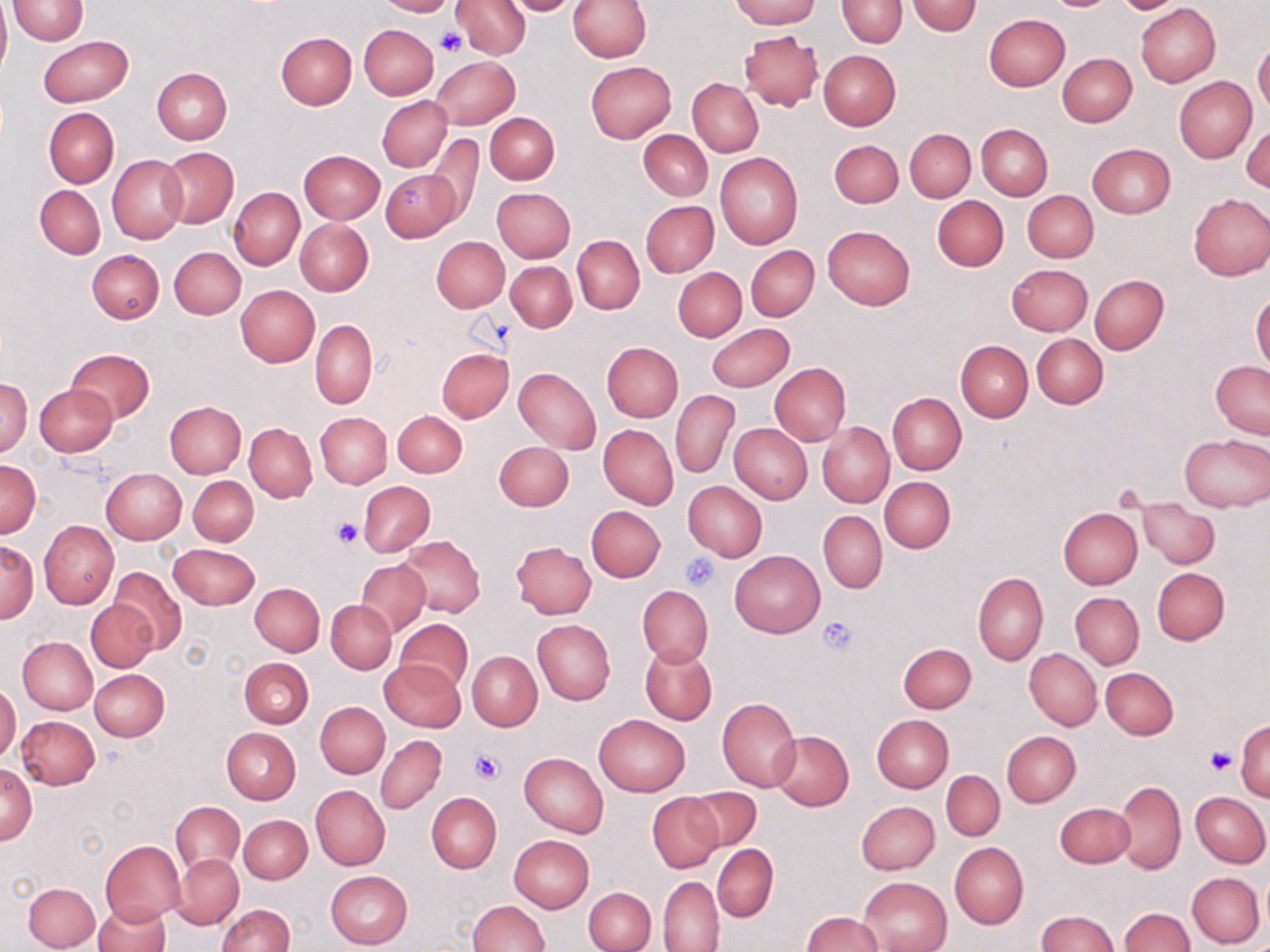
slide_level_diagnosis: negative for blood parasites
preparation: thin blood smear
stain: May-Grünwald-Giemsa
magnification: 1000x
image_size: 1270×952 pixels
field_of_view: one of a larger specimen
uninfected_red_blood_cell_locations: 'approximate bounding boxes as [x1, y1, x2, y2] in pixels: [9, 0, 88, 44], [374, 0, 457, 16], [452, 0, 530, 59], [500, 0, 584, 16], [568, 0, 651, 62], [729, 0, 819, 28], [837, 0, 907, 47], [1046, 0, 1113, 10], [0, 1, 10, 80], [906, 2, 982, 36], [1136, 3, 1220, 86], [984, 14, 1070, 91], [360, 24, 439, 99], [739, 29, 822, 109], [276, 32, 357, 110], [38, 35, 134, 107], [1253, 43, 1270, 116], [819, 50, 900, 130], [1058, 53, 1137, 127], [431, 56, 519, 129], [585, 60, 677, 143], [152, 68, 232, 144], [1173, 77, 1257, 162], [688, 78, 763, 156], [377, 95, 452, 171], [44, 108, 119, 187], [485, 113, 559, 184], [1243, 121, 1270, 192], [976, 124, 1052, 201], [905, 128, 976, 201], [638, 129, 712, 200], [425, 133, 483, 226], [829, 139, 903, 208], [1086, 143, 1175, 218], [160, 148, 238, 227], [299, 150, 385, 223], [715, 153, 803, 250], [107, 154, 187, 244], [380, 167, 464, 242], [35, 185, 105, 258], [229, 187, 303, 270], [492, 187, 575, 263], [1023, 190, 1097, 263], [1187, 193, 1270, 281], [932, 196, 1009, 271], [641, 200, 718, 278], [295, 219, 373, 296], [823, 225, 915, 309], [573, 235, 644, 314], [432, 237, 509, 312], [746, 246, 819, 320], [170, 247, 245, 319], [86, 249, 163, 323], [506, 261, 576, 332], [1007, 263, 1092, 335], [673, 267, 746, 342], [1090, 274, 1169, 354], [235, 285, 320, 366], [1251, 292, 1270, 374], [310, 319, 377, 409], [706, 323, 794, 391], [1032, 334, 1108, 408], [956, 340, 1032, 421], [602, 342, 683, 422], [436, 348, 513, 423], [67, 349, 155, 423], [1211, 361, 1270, 440], [769, 363, 850, 446], [514, 368, 601, 453], [1, 376, 32, 458], [35, 383, 117, 456], [671, 390, 738, 478], [887, 393, 966, 474], [165, 402, 246, 478], [394, 410, 467, 477], [315, 412, 391, 488], [245, 423, 317, 502], [817, 423, 894, 507], [729, 424, 812, 504], [599, 425, 678, 508], [1180, 434, 1270, 512], [494, 441, 573, 511], [1, 462, 40, 537], [102, 468, 186, 543], [189, 476, 258, 546], [879, 476, 956, 553], [359, 481, 435, 557], [683, 481, 767, 561], [1137, 498, 1219, 568], [586, 505, 665, 581], [1057, 507, 1142, 589], [819, 511, 887, 593], [39, 520, 118, 610], [396, 535, 486, 616], [510, 541, 597, 618], [1, 542, 39, 622], [170, 543, 259, 609], [730, 550, 825, 638], [356, 560, 429, 634], [110, 567, 185, 653], [1152, 567, 1229, 645], [973, 572, 1048, 667], [251, 583, 324, 656], [637, 585, 712, 668], [1070, 593, 1143, 668], [86, 599, 158, 672], [327, 600, 395, 674], [395, 618, 471, 691], [532, 620, 615, 704], [18, 636, 97, 714], [899, 642, 976, 713], [640, 644, 716, 725], [1025, 649, 1101, 731], [467, 651, 542, 730], [239, 658, 313, 728], [380, 659, 463, 731], [1100, 667, 1179, 740], [90, 668, 170, 741], [0, 684, 20, 763], [717, 698, 801, 791], [315, 701, 390, 777], [594, 714, 690, 796], [871, 714, 953, 792], [17, 715, 100, 789], [1236, 722, 1269, 800], [222, 727, 300, 804], [1003, 730, 1081, 806], [769, 731, 853, 811], [376, 735, 446, 814], [519, 752, 607, 838], [1, 762, 36, 846], [942, 770, 1004, 841], [1115, 781, 1186, 872], [311, 785, 390, 871], [686, 787, 762, 851], [1190, 791, 1269, 867], [648, 792, 723, 872], [427, 793, 501, 872], [856, 801, 940, 875], [172, 802, 244, 875], [1055, 803, 1134, 868], [238, 814, 312, 884], [509, 835, 594, 912], [101, 840, 186, 925], [949, 842, 1028, 928], [711, 845, 778, 921], [173, 854, 243, 928], [1259, 869, 1270, 937], [325, 870, 412, 949], [1187, 872, 1264, 947], [658, 876, 724, 951], [858, 877, 951, 952], [23, 882, 99, 951], [584, 887, 656, 952], [469, 899, 550, 952], [93, 901, 169, 952], [216, 904, 295, 952], [1119, 908, 1193, 952], [1036, 909, 1117, 952], [802, 910, 884, 952]'
modality: light microscopy
platelet_locations: 'approximate bounding boxes as [x1, y1, x2, y2] in pixels: [437, 28, 466, 56], [1114, 482, 1149, 511], [332, 518, 363, 549], [682, 553, 720, 591], [817, 616, 858, 655], [1204, 744, 1237, 775], [470, 748, 506, 783]'